Outline each blood parasite and name the species.
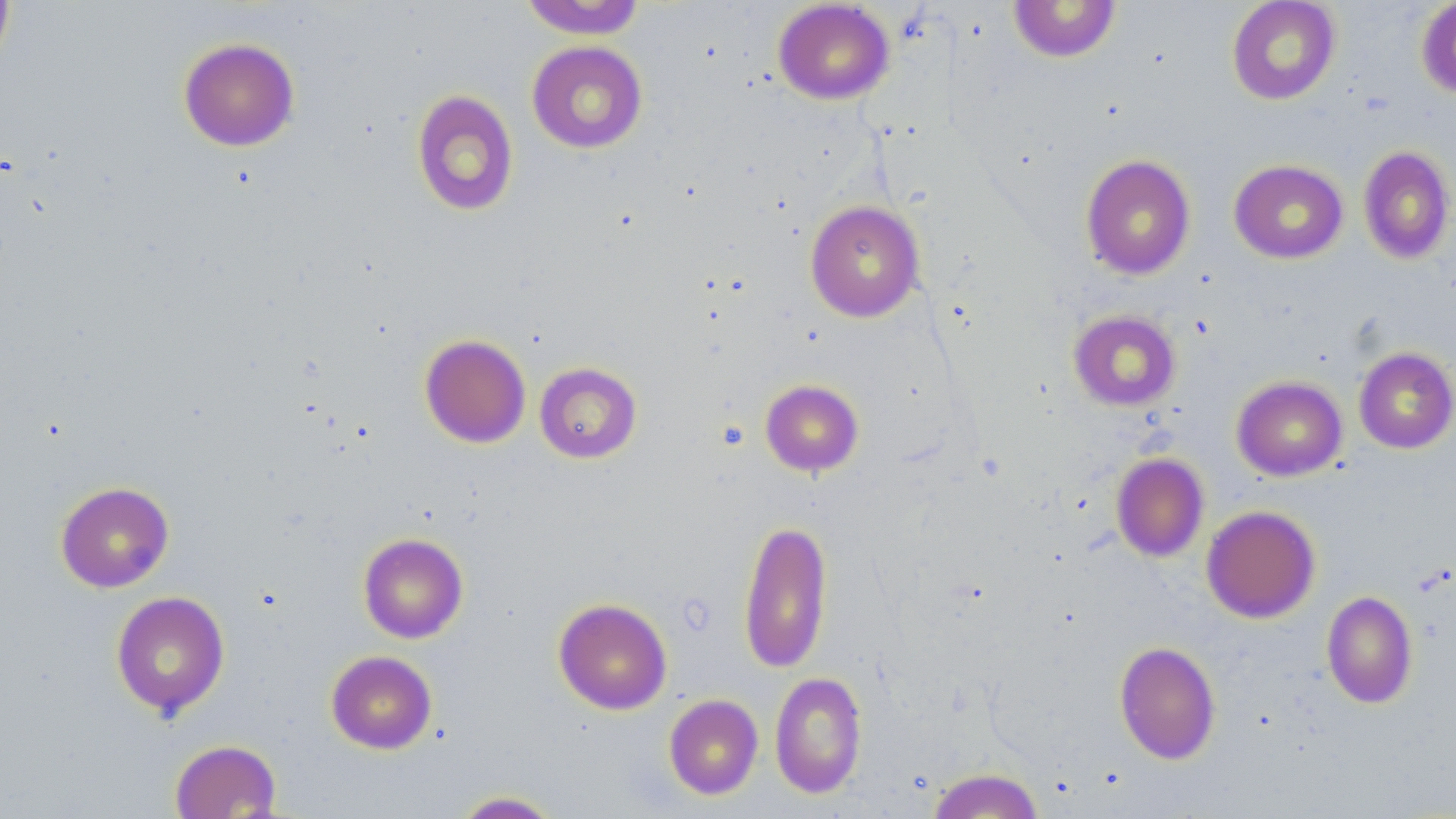

No blood parasites observed.

Approximate bounding boxes as (x1, y1, x2, y2) in pixels. Uninfected red blood cell locations: (0, 0, 16, 75), (519, 0, 647, 39), (1226, 0, 1342, 105), (1415, 0, 1456, 100), (772, 1, 894, 105), (1008, 1, 1122, 63), (178, 37, 300, 152), (526, 40, 648, 153), (411, 89, 519, 217), (1358, 145, 1455, 265), (1080, 154, 1196, 280), (1229, 159, 1348, 264), (805, 199, 925, 322), (1068, 309, 1181, 411), (419, 333, 531, 448), (1353, 346, 1456, 454), (534, 361, 643, 464), (1232, 376, 1347, 482), (760, 379, 864, 476), (1111, 452, 1209, 562), (55, 481, 174, 592), (1201, 505, 1321, 623), (737, 518, 834, 674), (357, 532, 469, 643), (111, 590, 230, 718), (1321, 590, 1418, 709), (553, 598, 672, 715), (1114, 641, 1221, 764), (325, 650, 437, 754), (770, 671, 867, 799), (663, 694, 763, 799), (169, 739, 281, 818), (927, 767, 1044, 818), (450, 790, 564, 818). Slide-level diagnosis: no evidence of blood parasites. May-Grünwald-Giemsa-stained preparation. Thin blood smear. Image is 1456×819 pixels. Light microscopy. One field of a larger specimen. 1000x magnification.